Locate every malaria parasite and every leukocyte.
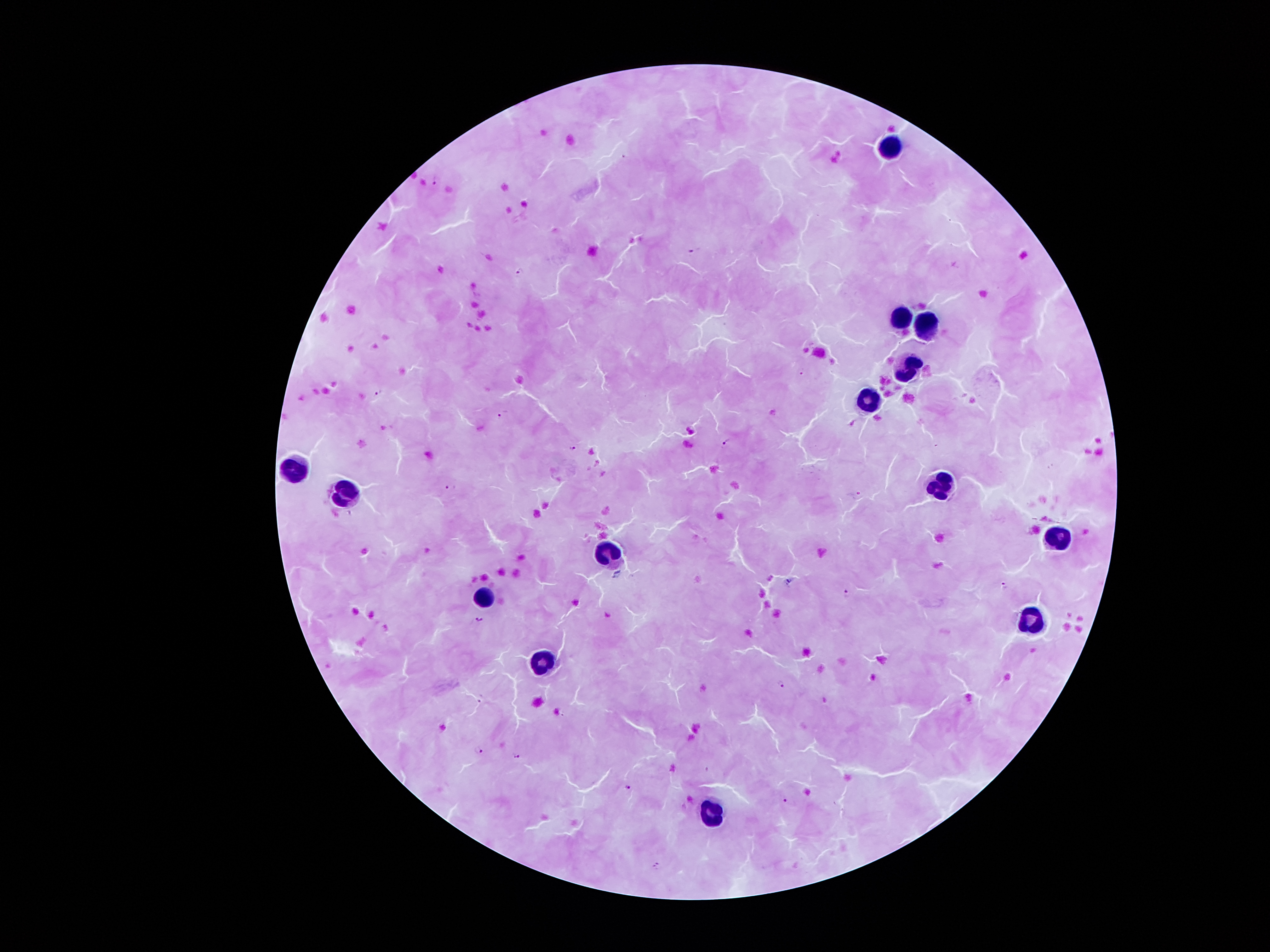
Approximate centers as (x, y) in pixels.
Malaria parasites: (435, 182), (694, 250), (520, 272), (802, 370), (379, 393), (503, 415), (726, 444), (572, 446), (450, 488), (1004, 586), (847, 593), (481, 620), (781, 684), (480, 751), (517, 756), (628, 788), (785, 801), (657, 865).
Leukocytes: (888, 148), (904, 318), (926, 327), (911, 367), (871, 402), (295, 468), (942, 482), (349, 491), (1056, 537), (610, 555), (484, 600), (1031, 622), (546, 662), (709, 814).

magnification: 100x
preparation: thick blood film
stain: Giemsa
field_of_view: one from this slide
image_size: 1270×952 pixels
patient_malaria_status: positive for Plasmodium falciparum
capture: smartphone through the microscope eyepiece